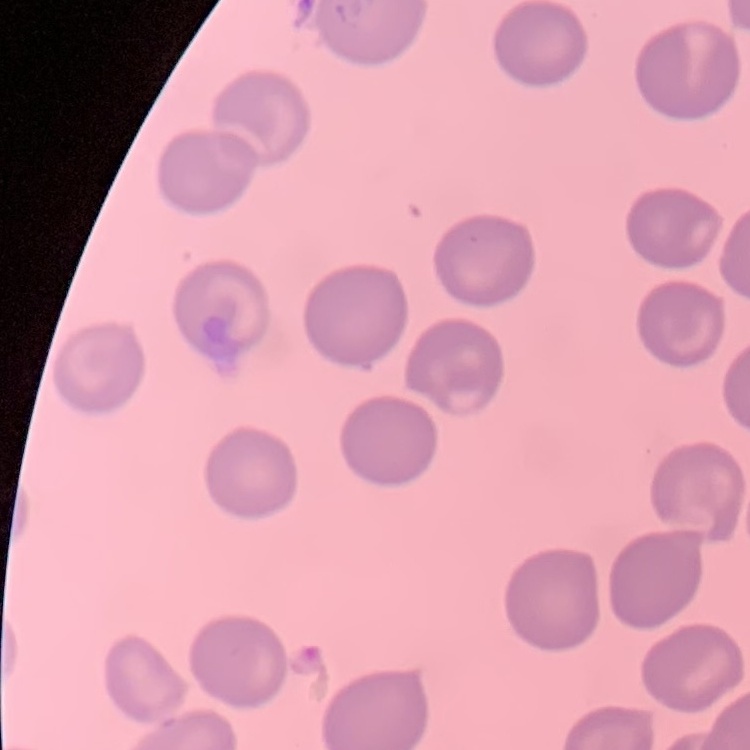 The red blood cells show no rouleaux formation. Square crop of a larger photomicrograph. Stained with either Field's or Giemsa. Thin blood smear.